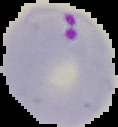

image_size: 118×127 pixels
image_type: cell region segmented out of the field of view; surrounding area masked to black
preparation: thin blood smear
result: Plasmodium parasites detected